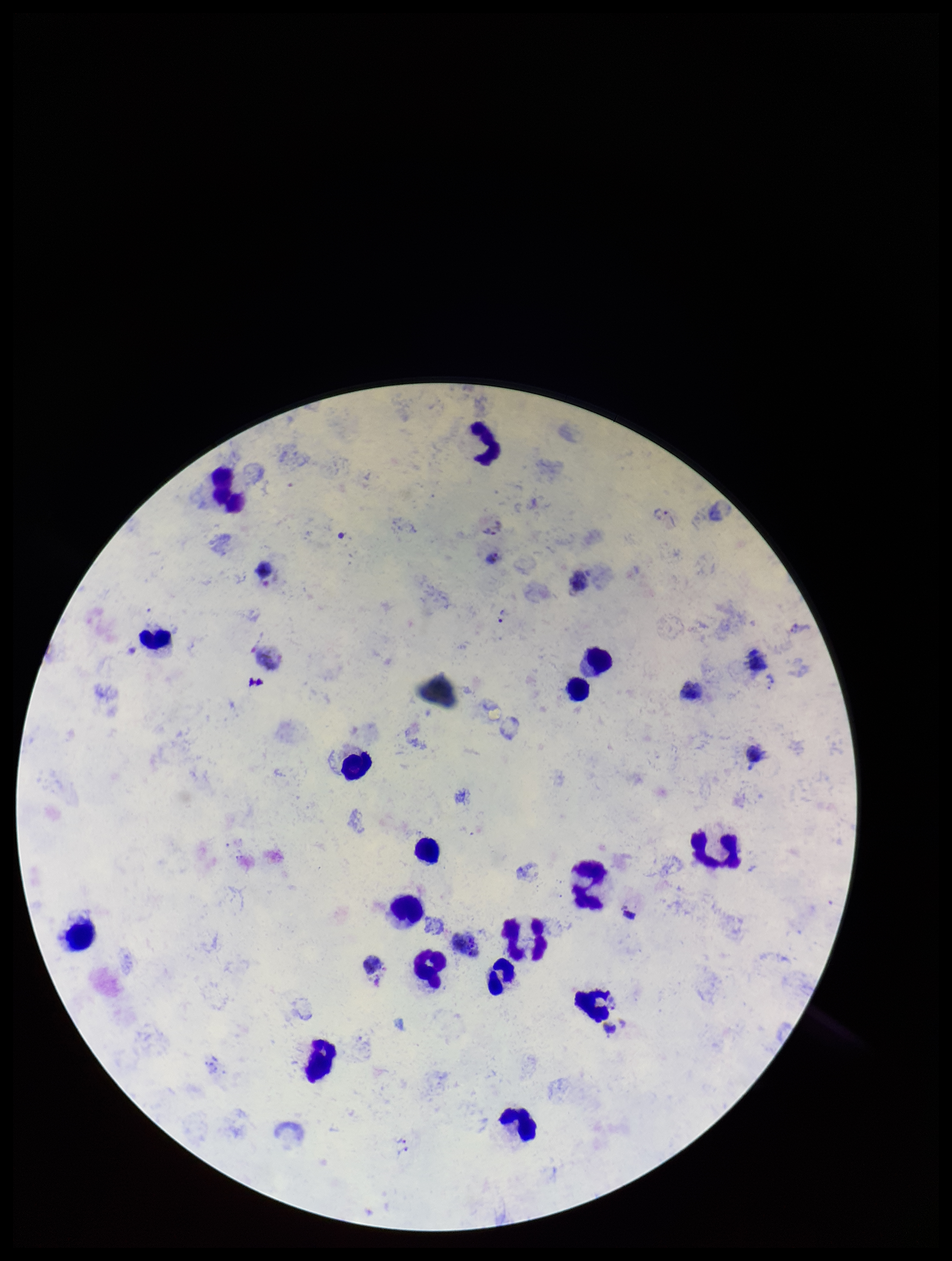
Summary:
  - Capture: smartphone photograph through the microscope eyepiece
  - Stain: Giemsa
  - Preparation: thick smear
  - Image size: 952×1261 pixels
  - Species reported for this patient: Plasmodium vivax
  - Parasite count: 1
  - Leukocyte count: 17
  - Field of view: one from this slide
  - Plasmodium parasites: detected
  - Patient malaria status: infected